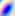
Summary:
  - Magnification: 400x
  - Identification: Toxoplasma gondii
  - Modality: micrograph